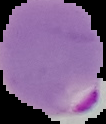
image size = 106×124 pixels
result = malaria parasites detected
preparation = thin blood film
image type = cell region segmented out of the field of view; surrounding area masked to black